Report the malaria status of this cell.
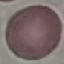
Uninfected.

Giemsa-stained preparation. Thin blood smear. Cell patch, automatically extracted from a larger field of view and resized to 64 × 64 pixels. Photographed with a smartphone camera at the microscope eyepiece.